Classify this cell by malaria status.
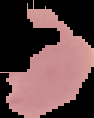

Uninfected.

Summary:
  - Preparation: thin blood smear
  - Image type: segmented cell region on a black background
  - Image size: 94×118 pixels